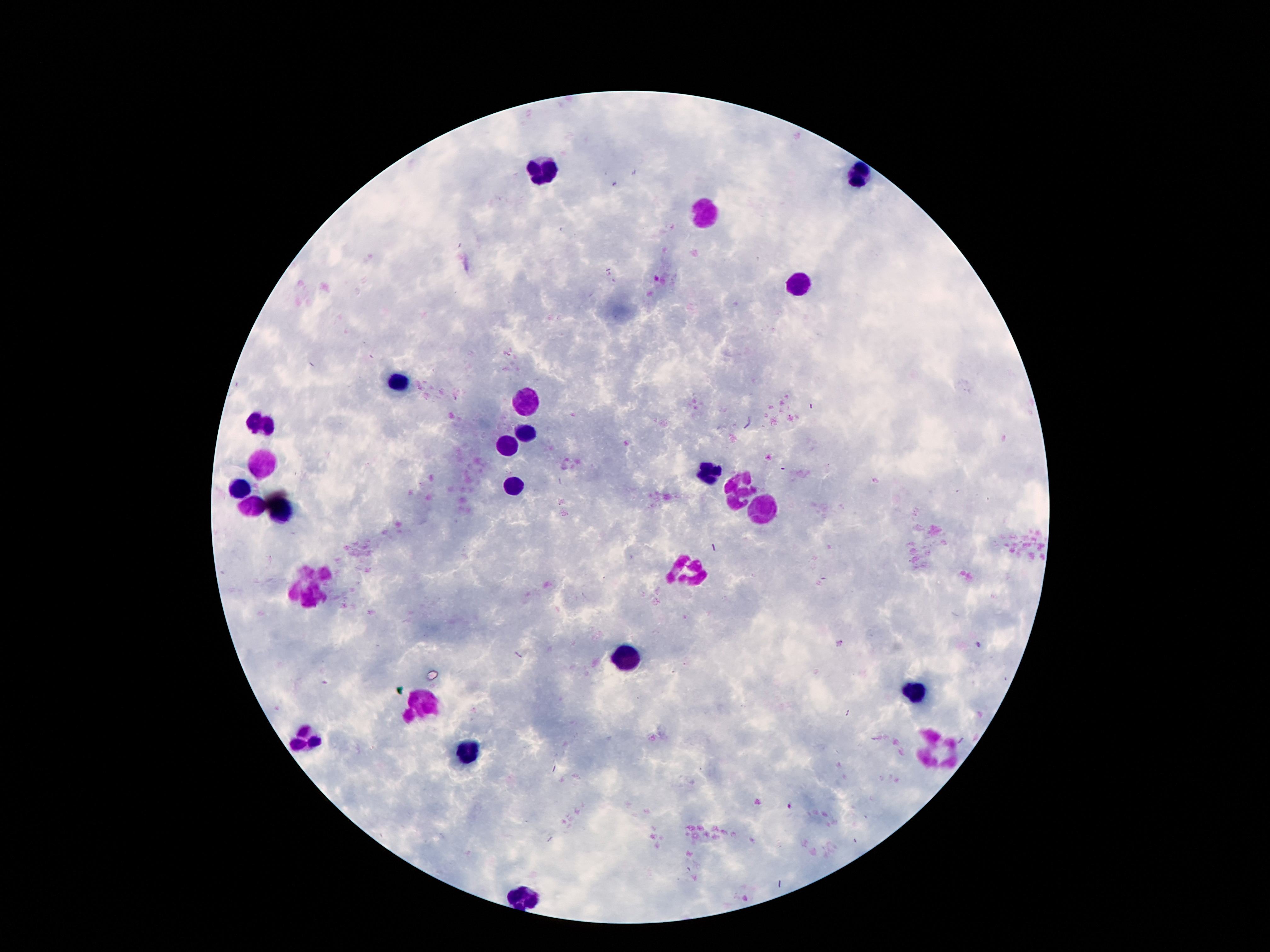
Approximate centers as (x, y) in pixels.
Summary:
  - Leukocyte locations: (549, 169), (860, 173), (709, 216), (799, 286), (393, 382), (524, 401), (262, 421), (526, 433), (506, 446), (260, 460), (711, 470), (514, 487), (239, 489), (737, 493), (249, 505), (278, 513), (762, 513), (686, 569), (313, 585), (633, 653), (915, 695), (420, 704), (309, 737), (940, 749), (467, 755), (520, 899)
  - Image size: 1270×952 pixels
  - Patient malaria status: not infected
  - Field of view: one from this slide
  - Stain: Giemsa
  - Capture: smartphone camera through the microscope eyepiece
  - Magnification: 100x
  - Preparation: thick blood film